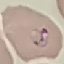

malaria status = parasitized
image type = cell patch, automatically extracted from a larger field of view and resized to 64 × 64 pixels
stain = Giemsa
capture = smartphone camera at the microscope eyepiece
preparation = thin smear